Outline each Plasmodium malariae-infected red blood cell.
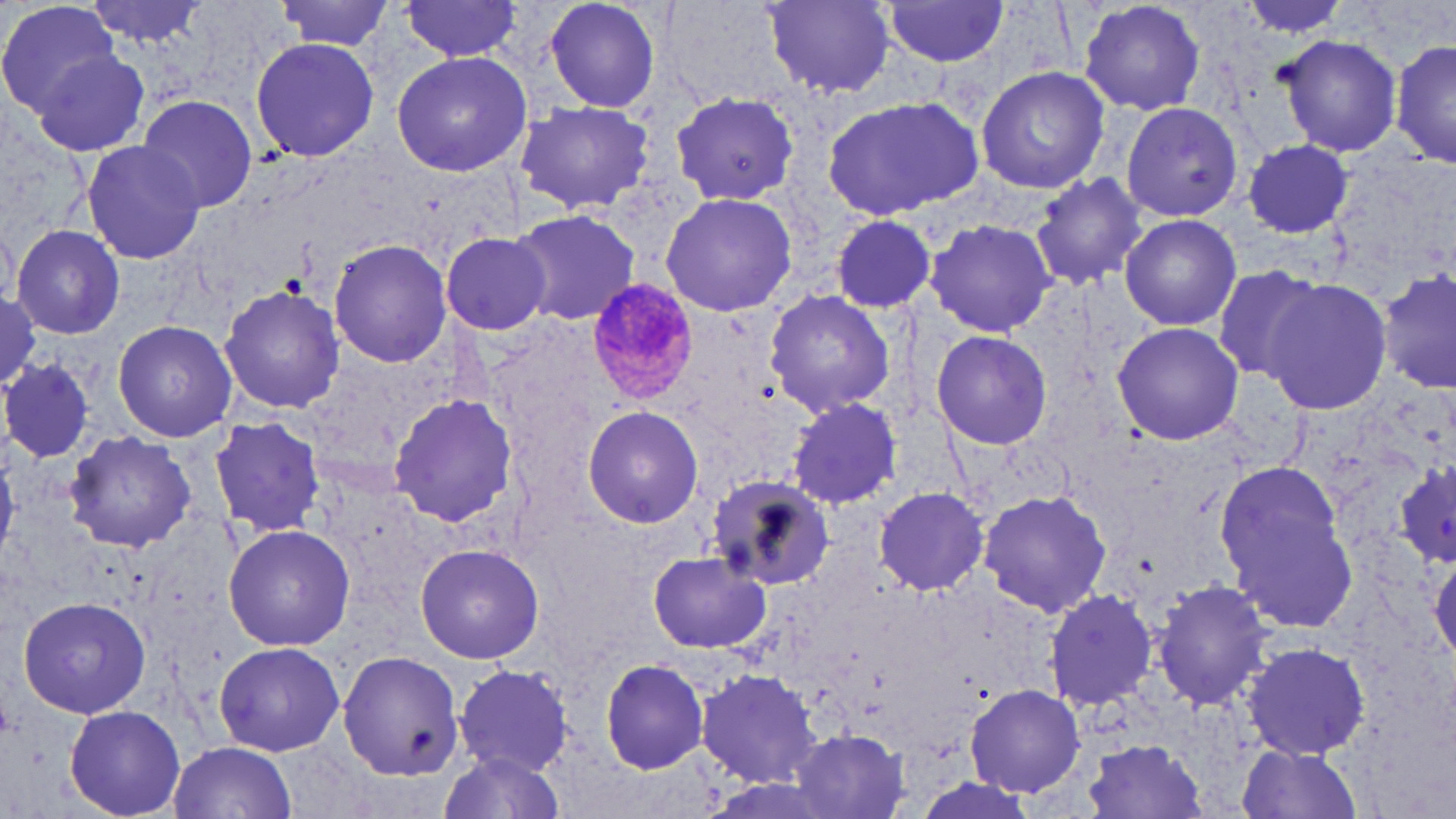

Approximate bounding boxes as named x1/y1/x2/y2 corners in pixels.
Plasmodium malariae-infected red blood cells: (x1=586, y1=281, x2=698, y2=407).

Uninfected red blood cell locations: (x1=86, y1=0, x2=217, y2=45), (x1=277, y1=0, x2=397, y2=53), (x1=543, y1=0, x2=663, y2=114), (x1=0, y1=1, x2=124, y2=115), (x1=399, y1=1, x2=523, y2=62), (x1=762, y1=1, x2=899, y2=97), (x1=1077, y1=1, x2=1209, y2=115), (x1=1234, y1=1, x2=1358, y2=37), (x1=882, y1=2, x2=1011, y2=67), (x1=1278, y1=32, x2=1402, y2=158), (x1=249, y1=37, x2=378, y2=162), (x1=1390, y1=38, x2=1454, y2=170), (x1=29, y1=47, x2=152, y2=156), (x1=390, y1=51, x2=531, y2=175), (x1=976, y1=65, x2=1109, y2=195), (x1=671, y1=92, x2=802, y2=206), (x1=822, y1=94, x2=986, y2=221), (x1=135, y1=95, x2=258, y2=213), (x1=512, y1=100, x2=659, y2=214), (x1=1122, y1=101, x2=1245, y2=220), (x1=80, y1=138, x2=205, y2=265), (x1=1241, y1=141, x2=1360, y2=238), (x1=1028, y1=175, x2=1151, y2=290), (x1=660, y1=190, x2=799, y2=318), (x1=508, y1=207, x2=639, y2=328), (x1=1118, y1=213, x2=1241, y2=330), (x1=829, y1=214, x2=938, y2=313), (x1=926, y1=218, x2=1059, y2=338), (x1=10, y1=222, x2=126, y2=341), (x1=441, y1=232, x2=551, y2=335), (x1=329, y1=238, x2=450, y2=367), (x1=1209, y1=264, x2=1324, y2=382), (x1=1378, y1=267, x2=1456, y2=394), (x1=1258, y1=274, x2=1391, y2=414), (x1=219, y1=282, x2=344, y2=415), (x1=764, y1=289, x2=894, y2=418), (x1=0, y1=293, x2=42, y2=394), (x1=113, y1=320, x2=237, y2=443), (x1=1112, y1=321, x2=1245, y2=445), (x1=928, y1=328, x2=1054, y2=449), (x1=0, y1=358, x2=95, y2=463), (x1=388, y1=394, x2=517, y2=527), (x1=786, y1=398, x2=904, y2=509), (x1=583, y1=407, x2=704, y2=529), (x1=209, y1=416, x2=327, y2=536), (x1=65, y1=432, x2=196, y2=552), (x1=1395, y1=456, x2=1456, y2=570), (x1=1213, y1=460, x2=1356, y2=634), (x1=705, y1=474, x2=835, y2=591), (x1=871, y1=486, x2=991, y2=595), (x1=979, y1=488, x2=1111, y2=617), (x1=222, y1=523, x2=355, y2=650), (x1=415, y1=543, x2=544, y2=665), (x1=647, y1=551, x2=770, y2=653), (x1=1428, y1=553, x2=1456, y2=665), (x1=1152, y1=577, x2=1273, y2=713), (x1=1042, y1=588, x2=1159, y2=712), (x1=17, y1=595, x2=151, y2=718), (x1=1238, y1=639, x2=1372, y2=759), (x1=215, y1=641, x2=345, y2=755), (x1=341, y1=651, x2=464, y2=778), (x1=600, y1=658, x2=710, y2=774), (x1=454, y1=663, x2=574, y2=775), (x1=697, y1=668, x2=818, y2=784), (x1=966, y1=683, x2=1088, y2=799), (x1=63, y1=705, x2=187, y2=819), (x1=790, y1=730, x2=911, y2=817), (x1=1080, y1=739, x2=1211, y2=819), (x1=168, y1=740, x2=297, y2=819), (x1=1232, y1=742, x2=1363, y2=819), (x1=436, y1=749, x2=564, y2=819). Slide-level diagnosis: Plasmodium malariae. May-Grünwald-Giemsa stain. Image is 1456×819 pixels. Light microscopy. Thin blood film. 1000x magnification. One field of a larger specimen.